Describe the morphology of the erythrocytes.
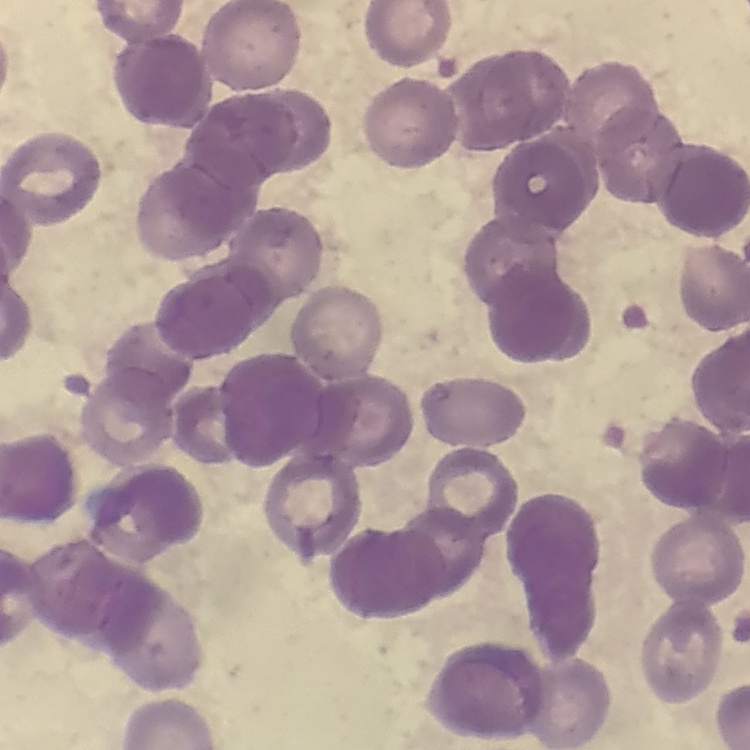

They show rouleaux formation.

Thin peripheral smear. Square crop of a larger photomicrograph. Stained with either Field's or Giemsa.